Identify the blood parasite species.
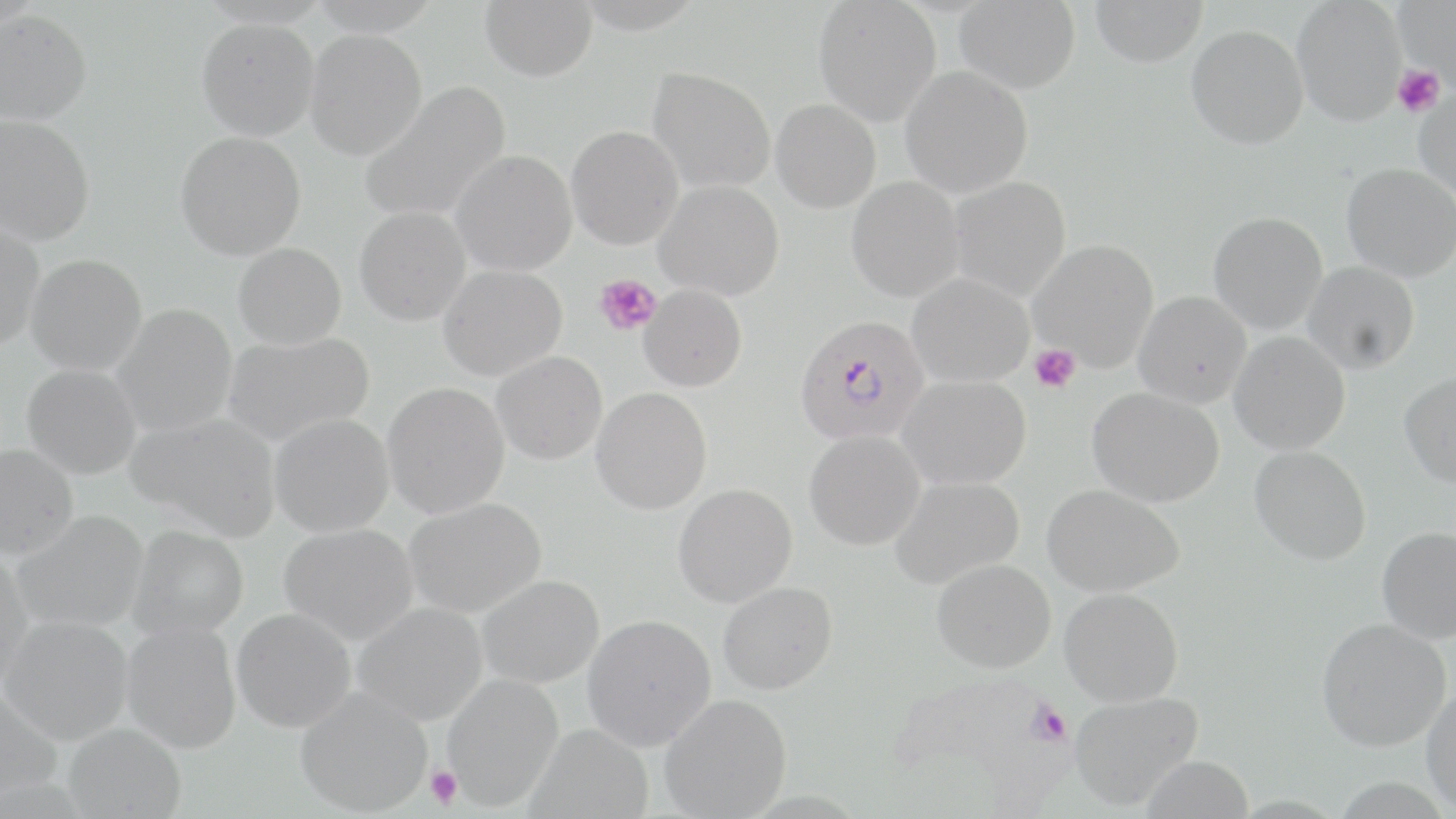

Plasmodium falciparum.

Summary:
  - Coordinate format: approximate bounding boxes as named x1/y1/x2/y2 corners in pixels
  - Plasmodium falciparum-infected red blood cell locations: (x1=794, y1=315, x2=930, y2=445)
  - Platelet locations: (x1=1392, y1=65, x2=1445, y2=118), (x1=594, y1=273, x2=661, y2=336), (x1=1029, y1=344, x2=1081, y2=392), (x1=425, y1=764, x2=463, y2=811)
  - Uninfected red blood cell locations: (x1=480, y1=0, x2=597, y2=82), (x1=813, y1=0, x2=941, y2=126), (x1=955, y1=0, x2=1079, y2=94), (x1=1089, y1=0, x2=1208, y2=67), (x1=1292, y1=0, x2=1407, y2=126), (x1=1394, y1=0, x2=1456, y2=85), (x1=0, y1=10, x2=92, y2=126), (x1=197, y1=17, x2=319, y2=141), (x1=1187, y1=24, x2=1308, y2=150), (x1=305, y1=29, x2=427, y2=160), (x1=901, y1=66, x2=1033, y2=198), (x1=647, y1=67, x2=776, y2=193), (x1=359, y1=82, x2=511, y2=224), (x1=1413, y1=86, x2=1456, y2=200), (x1=771, y1=99, x2=881, y2=213), (x1=0, y1=114, x2=95, y2=245), (x1=566, y1=126, x2=683, y2=250), (x1=176, y1=132, x2=306, y2=260), (x1=450, y1=151, x2=577, y2=276), (x1=1341, y1=163, x2=1456, y2=281), (x1=846, y1=177, x2=964, y2=302), (x1=949, y1=177, x2=1071, y2=300), (x1=655, y1=180, x2=784, y2=300), (x1=354, y1=206, x2=471, y2=326), (x1=1208, y1=211, x2=1328, y2=334), (x1=0, y1=218, x2=44, y2=351), (x1=1029, y1=240, x2=1159, y2=372), (x1=233, y1=242, x2=346, y2=349), (x1=26, y1=254, x2=147, y2=375), (x1=1303, y1=261, x2=1420, y2=374), (x1=438, y1=265, x2=567, y2=381), (x1=907, y1=274, x2=1034, y2=387), (x1=639, y1=285, x2=747, y2=392), (x1=1134, y1=290, x2=1252, y2=407), (x1=111, y1=304, x2=238, y2=436), (x1=221, y1=331, x2=374, y2=447), (x1=1229, y1=331, x2=1350, y2=456), (x1=491, y1=351, x2=607, y2=465), (x1=21, y1=364, x2=141, y2=480), (x1=1399, y1=372, x2=1456, y2=488), (x1=899, y1=375, x2=1031, y2=489), (x1=382, y1=383, x2=509, y2=519), (x1=591, y1=387, x2=712, y2=516), (x1=1088, y1=387, x2=1225, y2=507), (x1=124, y1=411, x2=281, y2=541), (x1=269, y1=414, x2=394, y2=537), (x1=804, y1=430, x2=925, y2=550), (x1=1, y1=444, x2=79, y2=560), (x1=1250, y1=446, x2=1372, y2=565), (x1=890, y1=475, x2=1024, y2=588), (x1=673, y1=483, x2=797, y2=607), (x1=1042, y1=484, x2=1185, y2=597), (x1=404, y1=498, x2=547, y2=618), (x1=11, y1=511, x2=148, y2=634), (x1=279, y1=523, x2=418, y2=645), (x1=128, y1=524, x2=248, y2=641), (x1=1377, y1=527, x2=1456, y2=644), (x1=0, y1=552, x2=35, y2=690), (x1=932, y1=559, x2=1056, y2=673), (x1=477, y1=576, x2=605, y2=689), (x1=717, y1=582, x2=837, y2=695), (x1=1060, y1=587, x2=1184, y2=707), (x1=354, y1=602, x2=487, y2=726), (x1=231, y1=609, x2=356, y2=733), (x1=1, y1=614, x2=133, y2=745), (x1=582, y1=614, x2=717, y2=751), (x1=1316, y1=618, x2=1451, y2=752), (x1=121, y1=621, x2=242, y2=754), (x1=443, y1=674, x2=563, y2=811), (x1=0, y1=683, x2=62, y2=807), (x1=1421, y1=684, x2=1456, y2=815), (x1=295, y1=687, x2=432, y2=817), (x1=1070, y1=691, x2=1204, y2=810), (x1=660, y1=693, x2=791, y2=818), (x1=62, y1=723, x2=186, y2=818), (x1=527, y1=724, x2=654, y2=817)
  - Magnification: 1000x
  - Field of view: single
  - Preparation: thin blood smear
  - Image size: 1456×819 pixels
  - Modality: optical microscopy
  - Stain: May-Grünwald-Giemsa